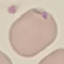

Malaria status: parasitized. Giemsa stain. Acquired by smartphone through the microscope eyepiece. Automatically extracted cell patch, resized to 64 × 64 pixels. Thin smear of blood.